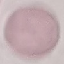
Malaria status: uninfected. Giemsa stain. Automatically extracted cell patch, resized to 64 × 64 pixels. Thin blood smear. Acquired by smartphone through the microscope eyepiece.